Classify this cell by malaria status.
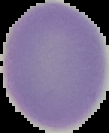

It is uninfected.

image type = cell region segmented out of the field of view; surrounding area masked to black
preparation = thin blood smear
image size = 109×133 pixels